Classify this cell by malaria status.
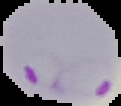

It is parasitized.

Summary:
  - Image type: cell region segmented out of the field of view; surrounding area masked to black
  - Image size: 121×106 pixels
  - Preparation: thin blood film